Assess this cell for malaria.
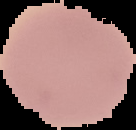
It is uninfected.

Summary:
  - Image size: 136×130 pixels
  - Image type: segmented cell region on a black background
  - Preparation: thin blood smear